Give the position of every Plasmodium parasite visible.
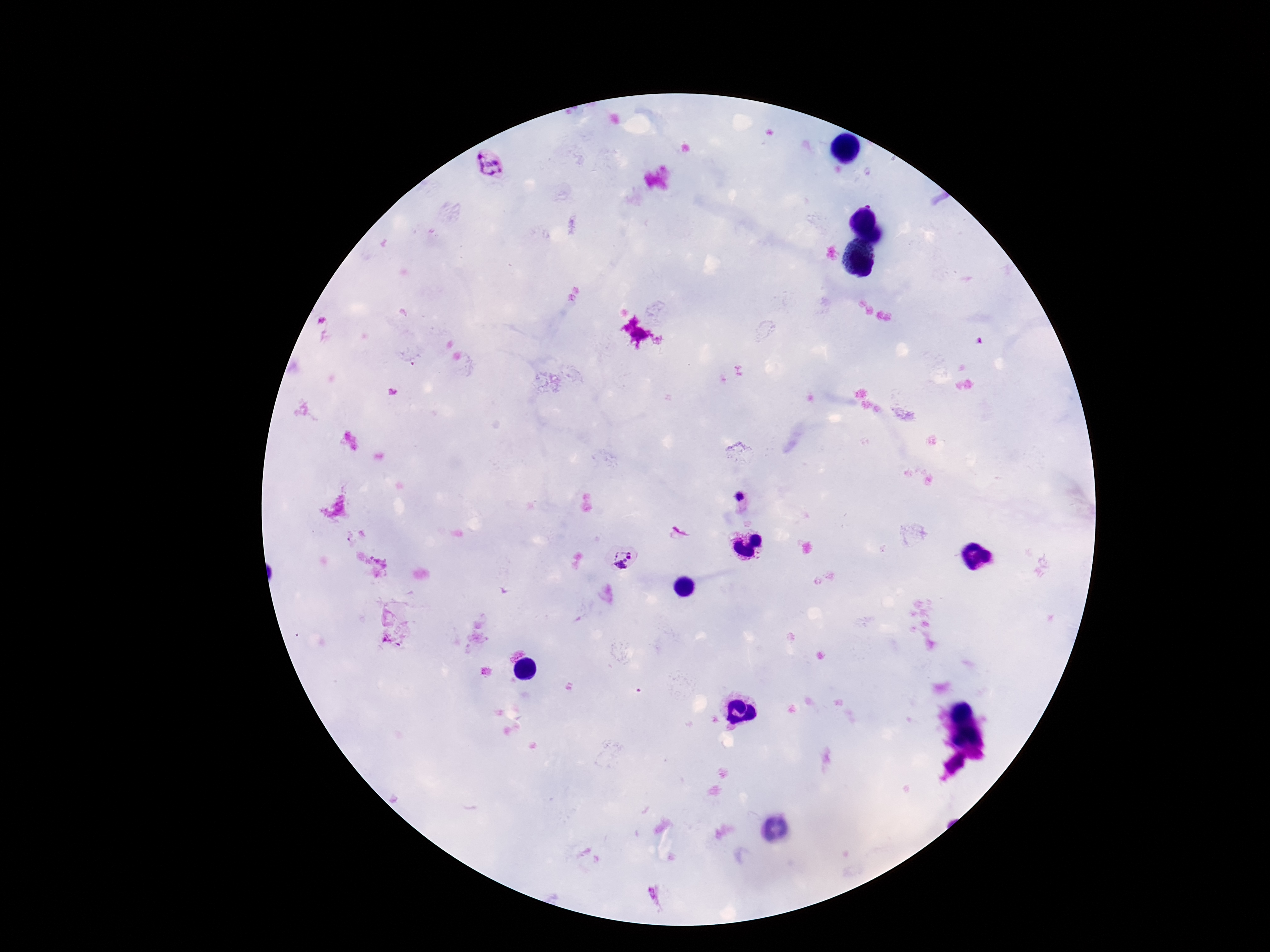

Approximate centers as (x, y) in pixels.
Plasmodium parasites: (739, 499), (622, 554).

Summary:
  - Preparation: thick blood film
  - Magnification: 100x
  - Field of view: one from this slide
  - Stain: Giemsa
  - Image size: 1270×952 pixels
  - Patient malaria status: positive
  - Capture: smartphone camera through the microscope eyepiece